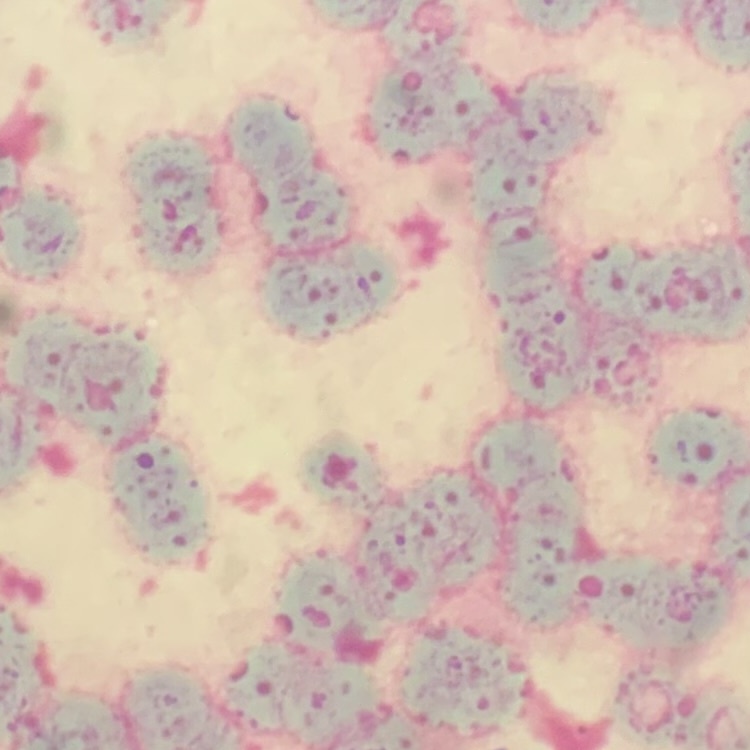
erythrocyte_morphology: rouleaux formation
image_type: square crop of a larger photomicrograph
preparation: thin blood smear
stain: Field's or Giemsa